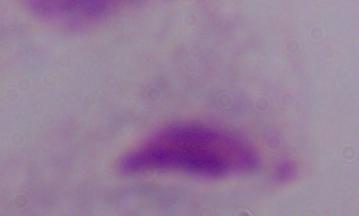

Summary:
  - Identification: trichomonad
  - Modality: photomicrograph
  - Magnification: 1000x